Describe the morphology of the erythrocytes.
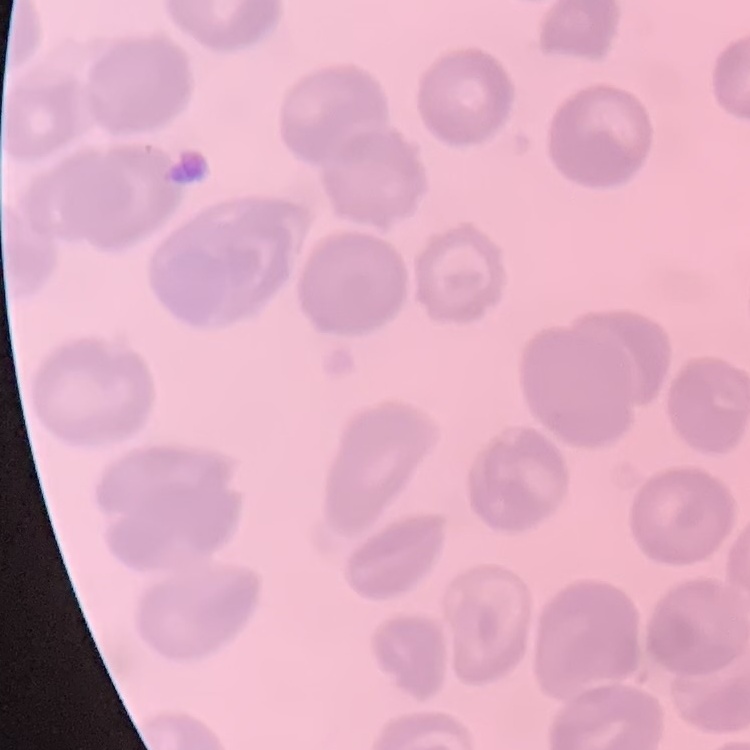

They show no rouleaux formation.

Square crop of a larger photomicrograph. Stained with either Field's or Giemsa. Thin blood smear.